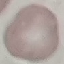 Malaria status: uninfected. Cell patch, automatically extracted from a larger field of view and resized to 64 × 64 pixels. Thin smear of blood. Acquired by smartphone through the microscope eyepiece. Giemsa-stained preparation.